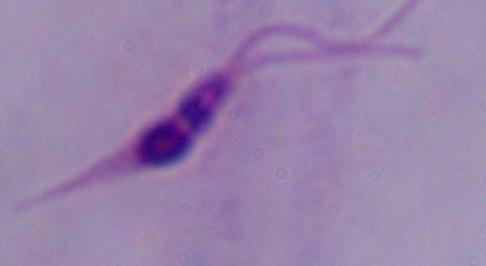

modality = micrograph
magnification = 1000x
identification = Leishmania